Classify this cell by malaria status.
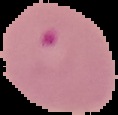
It is parasitized.

preparation: thin blood smear
image_size: 118×115 pixels
image_type: segmented cell region on a black background